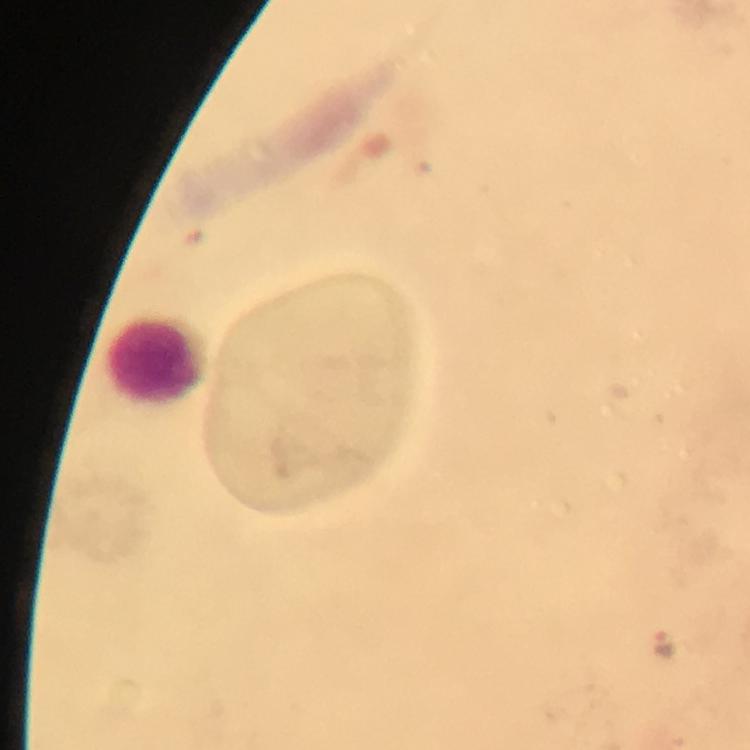
context = from a diagnostic examination for malaria
stain = Giemsa
image size = 750×750 pixels
immersion oil = used
capture = smartphone mounted on the microscope
preparation = thick smear
cropped from = a single field of view
leukocyte locations = approximate centers as [x, y] in pixels: [155, 359]
Plasmodium parasite locations = approximate centers as [x, y] in pixels: [663, 641]
magnification = 100x